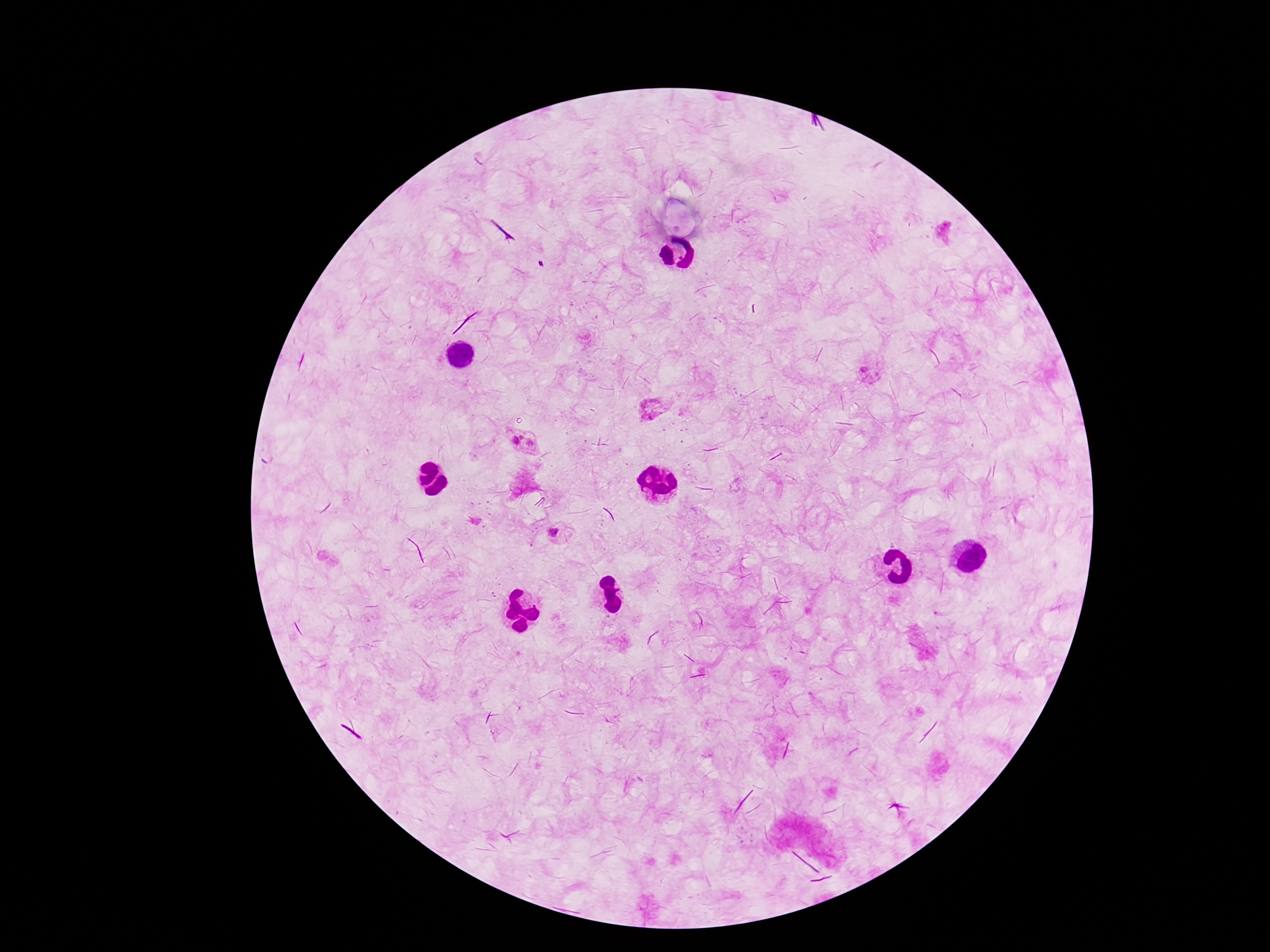 Approximate centers as [x, y] in pixels. Plasmodium parasite locations: [864, 368], [654, 408], [522, 437], [515, 442], [532, 443], [554, 532]. One field from this slide. Thick blood smear. Patient malaria status: positive. Photographed through the microscope eyepiece with a smartphone camera. Giemsa-stained preparation. Image is 1270×952 pixels. 100x magnification.